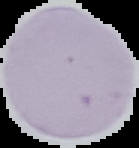 Image is 139×148 pixels. Segmented cell region on a black background. Malaria status: uninfected. From a thin blood smear.